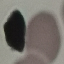 Malaria status: uninfected. Giemsa stain. Thin smear of blood. Cell patch, automatically extracted from a larger field of view and resized to 64 × 64 pixels. Photographed with a smartphone camera at the microscope eyepiece.